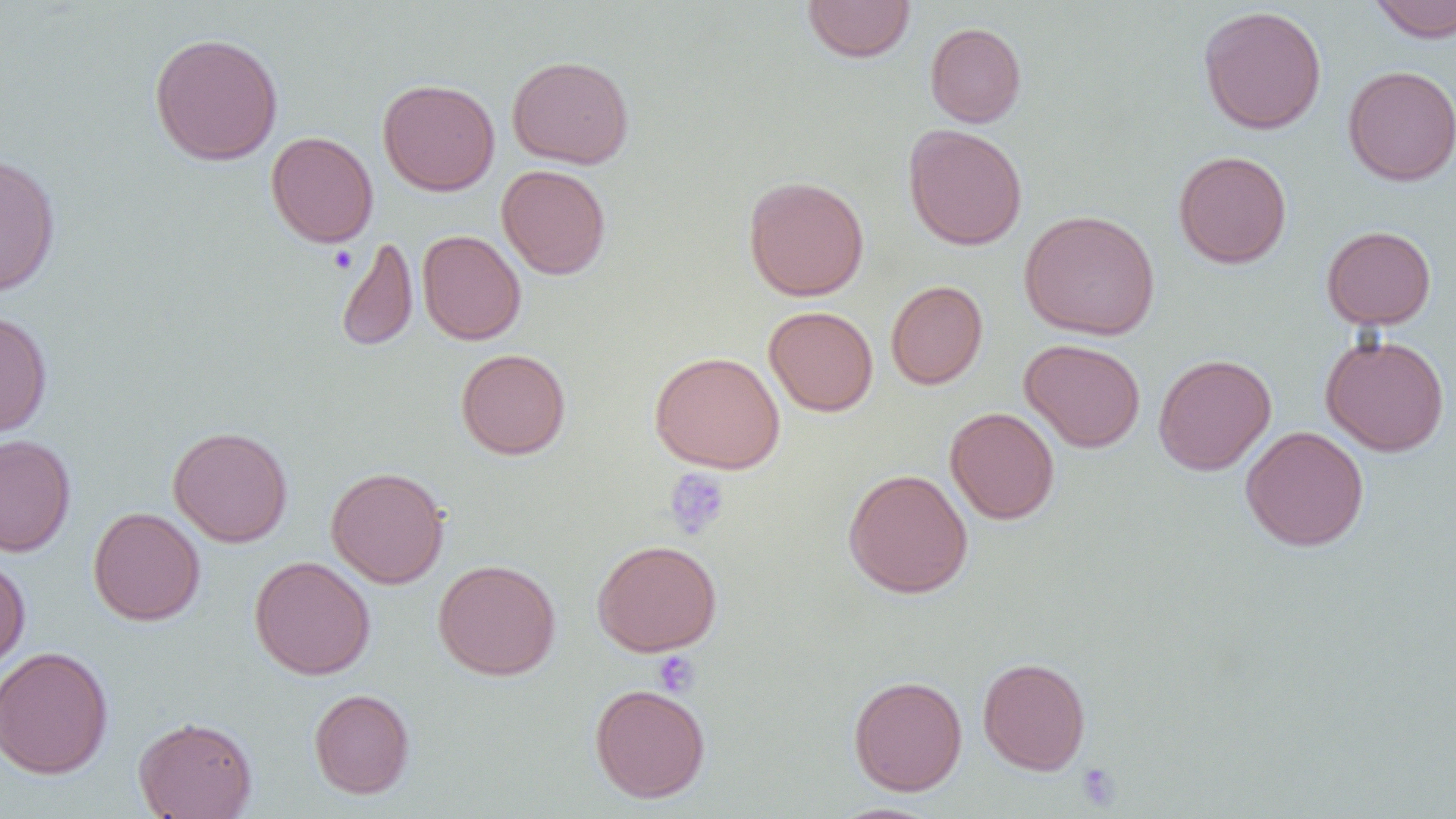

slide-level diagnosis = negative for blood parasites
uninfected red blood cell locations = approximate bounding boxes as named x1/y1/x2/y2 corners in pixels: (x1=1367, y1=0, x2=1456, y2=43), (x1=802, y1=1, x2=916, y2=63), (x1=1198, y1=5, x2=1327, y2=135), (x1=925, y1=22, x2=1027, y2=127), (x1=149, y1=32, x2=284, y2=165), (x1=506, y1=54, x2=634, y2=169), (x1=1342, y1=65, x2=1456, y2=186), (x1=377, y1=78, x2=500, y2=195), (x1=903, y1=124, x2=1028, y2=251), (x1=266, y1=131, x2=378, y2=247), (x1=1173, y1=150, x2=1292, y2=269), (x1=0, y1=152, x2=62, y2=297), (x1=497, y1=164, x2=611, y2=280), (x1=743, y1=175, x2=869, y2=301), (x1=1019, y1=209, x2=1160, y2=340), (x1=1321, y1=225, x2=1437, y2=330), (x1=417, y1=229, x2=527, y2=345), (x1=335, y1=237, x2=418, y2=351), (x1=886, y1=280, x2=988, y2=389), (x1=763, y1=305, x2=879, y2=417), (x1=0, y1=309, x2=53, y2=439), (x1=1320, y1=333, x2=1450, y2=456), (x1=1019, y1=338, x2=1146, y2=452), (x1=456, y1=348, x2=571, y2=460), (x1=649, y1=350, x2=785, y2=473), (x1=1153, y1=353, x2=1276, y2=476), (x1=945, y1=406, x2=1060, y2=524), (x1=168, y1=425, x2=293, y2=547), (x1=1240, y1=425, x2=1369, y2=551), (x1=0, y1=434, x2=76, y2=556), (x1=326, y1=466, x2=450, y2=589), (x1=843, y1=468, x2=973, y2=598), (x1=88, y1=506, x2=206, y2=626), (x1=592, y1=539, x2=723, y2=656), (x1=0, y1=555, x2=31, y2=673), (x1=249, y1=555, x2=376, y2=680), (x1=432, y1=558, x2=561, y2=681), (x1=0, y1=645, x2=114, y2=779), (x1=977, y1=656, x2=1091, y2=775), (x1=848, y1=675, x2=968, y2=796), (x1=589, y1=683, x2=711, y2=803), (x1=308, y1=688, x2=415, y2=799), (x1=133, y1=715, x2=258, y2=819)
image size = 1456×819 pixels
platelet locations = approximate bounding boxes as named x1/y1/x2/y2 corners in pixels: (x1=328, y1=246, x2=357, y2=274), (x1=664, y1=467, x2=731, y2=539), (x1=651, y1=650, x2=700, y2=697), (x1=1076, y1=762, x2=1122, y2=811)
preparation = thin blood smear
modality = optical microscopy
magnification = 1000x
field of view = one of a larger specimen